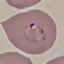

Malaria status: parasitized. Giemsa-stained preparation. Cell patch, automatically extracted from a larger field of view and resized to 64 × 64 pixels. Acquired by smartphone through the microscope eyepiece. Thin blood smear.